Assess this cell for malaria.
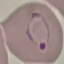

Parasitized.

Summary:
  - Capture: smartphone through the microscope eyepiece
  - Stain: Giemsa
  - Preparation: thin blood smear
  - Image type: cell patch, automatically extracted from a larger field of view and resized to 64 × 64 pixels